Locate every blood parasite and identify its species.
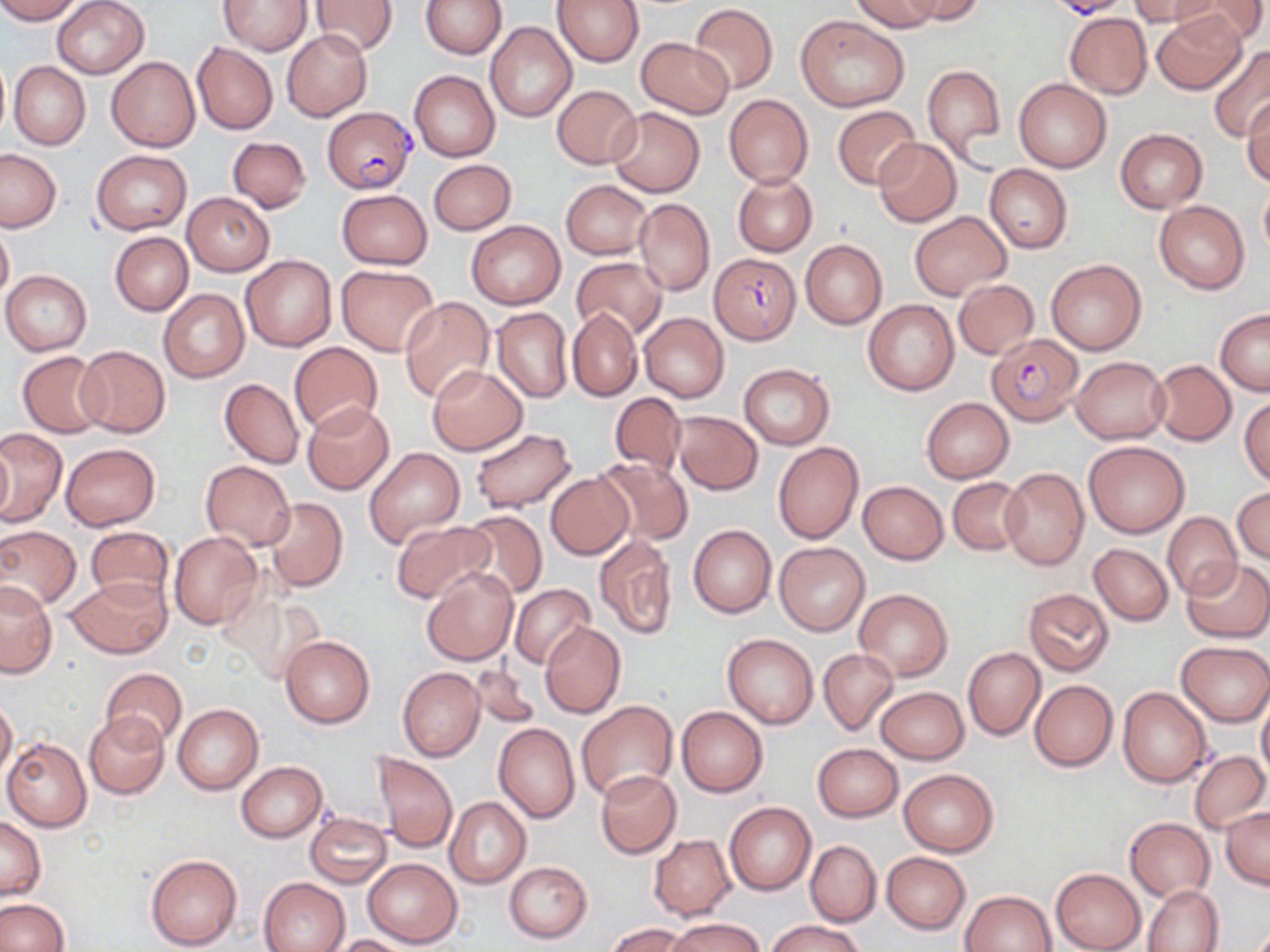

Approximate bounding boxes as [x1, y1, x2, y2] in pixels.
Plasmodium falciparum-infected red blood cells: [1056, 0, 1127, 22], [324, 106, 416, 192], [709, 253, 799, 343], [987, 331, 1082, 425].
No Plasmodium ovale, Plasmodium malariae, Plasmodium vivax, Babesia divergens, or Trypanosoma brucei observed.

Uninfected red blood cell locations: [0, 0, 83, 22], [52, 0, 150, 79], [220, 0, 312, 54], [419, 0, 506, 59], [552, 0, 643, 67], [849, 0, 942, 33], [904, 0, 984, 23], [1130, 0, 1220, 28], [1182, 0, 1266, 47], [309, 1, 399, 55], [689, 4, 777, 94], [1065, 12, 1153, 100], [1151, 12, 1247, 94], [796, 14, 909, 111], [484, 21, 577, 122], [281, 29, 372, 121], [636, 37, 734, 119], [192, 43, 278, 133], [1206, 45, 1270, 140], [106, 55, 201, 152], [8, 61, 91, 150], [922, 64, 1006, 166], [409, 70, 500, 161], [1013, 79, 1111, 172], [552, 85, 642, 168], [723, 94, 812, 188], [1243, 96, 1270, 187], [832, 106, 921, 190], [607, 107, 705, 197], [1116, 129, 1207, 213], [227, 136, 311, 212], [872, 138, 962, 228], [0, 148, 60, 232], [92, 149, 191, 234], [429, 159, 517, 235], [985, 164, 1073, 253], [733, 174, 816, 256], [562, 180, 650, 259], [1259, 187, 1270, 260], [336, 188, 433, 270], [182, 192, 274, 276], [634, 199, 714, 295], [1154, 200, 1250, 294], [910, 211, 1011, 300], [466, 219, 565, 309], [0, 221, 13, 308], [110, 232, 192, 315], [800, 240, 887, 329], [241, 255, 336, 351], [572, 257, 667, 340], [1046, 259, 1146, 355], [336, 265, 439, 356], [2, 270, 92, 355], [953, 278, 1038, 358], [158, 289, 249, 383], [398, 296, 496, 404], [863, 299, 959, 396], [492, 307, 573, 403], [568, 307, 642, 402], [1216, 308, 1270, 395], [640, 312, 729, 402], [290, 342, 382, 437], [75, 344, 171, 438], [17, 350, 108, 437], [1071, 356, 1170, 443], [1151, 360, 1235, 445], [739, 363, 835, 449], [427, 365, 527, 455], [219, 378, 303, 468], [608, 390, 688, 475], [921, 397, 1014, 483], [1239, 397, 1270, 485], [304, 402, 394, 494], [671, 411, 762, 494], [0, 428, 66, 526], [468, 428, 579, 514], [1, 437, 13, 524], [1084, 440, 1190, 537], [773, 441, 864, 545], [60, 443, 161, 531], [364, 447, 464, 548], [594, 457, 693, 546], [201, 462, 295, 550], [1001, 466, 1088, 570], [546, 473, 633, 559], [947, 477, 1027, 555], [858, 480, 948, 564], [1232, 487, 1270, 564], [262, 497, 348, 593], [460, 511, 547, 600], [1163, 513, 1243, 600], [390, 520, 493, 604], [687, 524, 776, 618], [85, 526, 174, 607], [0, 527, 80, 610], [168, 531, 263, 630], [594, 534, 678, 641], [774, 542, 869, 635], [1089, 543, 1173, 625], [1182, 557, 1270, 643], [422, 567, 520, 665], [66, 576, 172, 658], [0, 579, 57, 679], [509, 583, 595, 669], [854, 589, 953, 680], [1023, 589, 1114, 676], [540, 622, 625, 718], [722, 633, 818, 728], [280, 635, 374, 729], [1177, 641, 1270, 725], [963, 647, 1044, 741], [819, 648, 900, 737], [468, 663, 540, 730], [398, 667, 484, 760], [99, 668, 187, 752], [1029, 680, 1118, 772], [1117, 686, 1213, 788], [876, 687, 968, 764], [1257, 693, 1270, 779], [0, 698, 18, 783], [577, 700, 678, 801], [173, 704, 263, 794], [676, 706, 768, 797], [84, 713, 171, 800], [494, 723, 580, 823], [2, 737, 93, 830], [813, 744, 903, 821], [374, 751, 457, 853], [1188, 751, 1270, 834], [236, 761, 328, 842], [899, 769, 997, 856], [595, 770, 681, 857], [444, 797, 531, 888], [724, 801, 816, 895], [1221, 808, 1270, 890], [304, 812, 392, 889], [1, 817, 45, 901], [1125, 817, 1215, 902], [649, 835, 735, 920], [806, 841, 881, 928], [881, 851, 970, 935], [145, 853, 242, 950], [363, 859, 461, 947], [503, 861, 592, 943], [1051, 868, 1145, 952], [260, 876, 349, 952], [1142, 884, 1223, 952], [961, 890, 1057, 952], [0, 898, 70, 951], [668, 917, 764, 952], [767, 919, 867, 952], [607, 922, 689, 952], [331, 934, 418, 952]. Slide-level diagnosis: Plasmodium falciparum. Image is 1270×952 pixels. Thin blood film. May-Grünwald-Giemsa stain. Optical microscopy. 1000x magnification. Single field of view.